Assess for Plasmodium parasites.
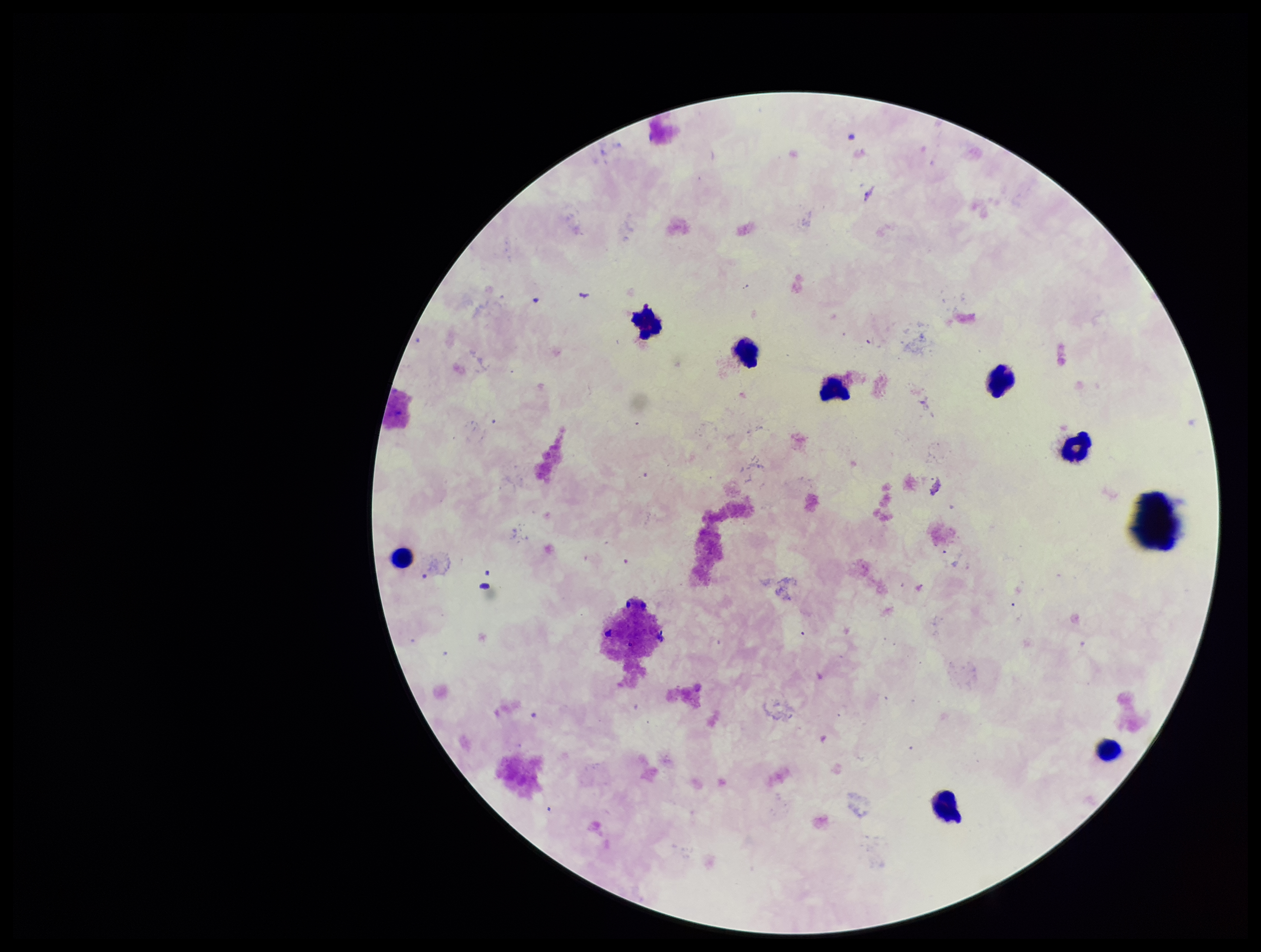
None detected.

Summary:
  - Patient malaria status: negative
  - Preparation: thick blood smear
  - Image size: 1261×952 pixels
  - Stain: Giemsa
  - Parasite count: 0
  - Leukocyte count: 8
  - Capture: smartphone photograph through the microscope eyepiece
  - Field of view: one from this slide